Assess the morphology of the erythrocytes.
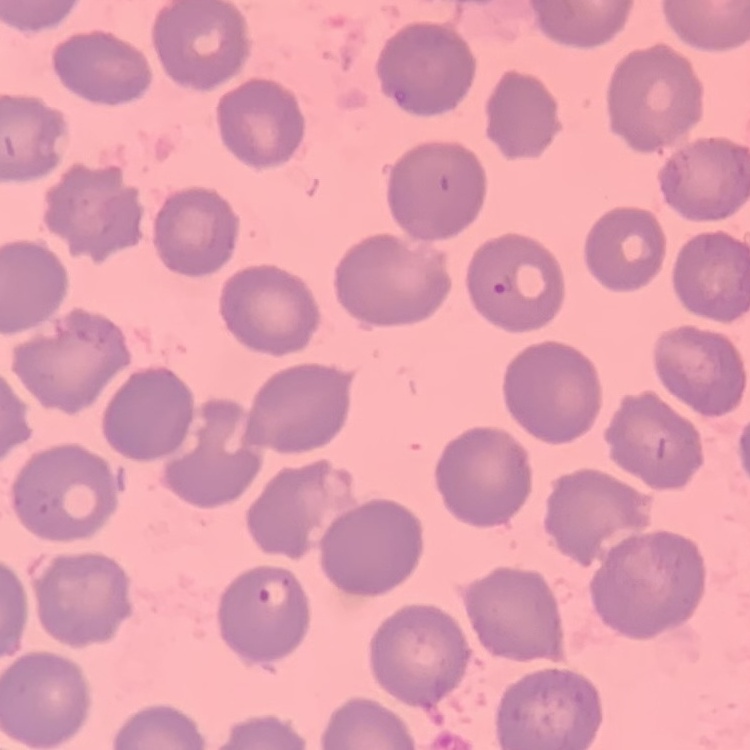

No rouleaux formation.

Summary:
  - Image type: one tile cut from a larger photomicrograph
  - Stain: Field's or Giemsa
  - Preparation: thin blood film